State which parasite is depicted.
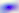
Toxoplasma gondii.

magnification = 400x
modality = photomicrograph